Classify this cell by malaria status.
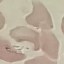
It is uninfected.

Automatically extracted cell patch, resized to 64 × 64 pixels. Photographed with a smartphone camera at the microscope eyepiece. Giemsa stain. Thin blood film.